Classify this cell by malaria status.
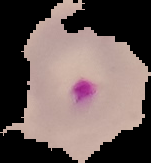

It is parasitized.

Summary:
  - Preparation: thin blood smear
  - Image size: 151×163 pixels
  - Image type: segmented cell region with the area outside set to black